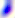
Summary:
  - Modality: photomicrograph
  - Identification: Toxoplasma gondii
  - Magnification: 400x